Report the malaria status of this cell.
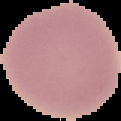

It is uninfected.

From a thin blood film. Segmented cell region on a black background. Image is 121×121 pixels.